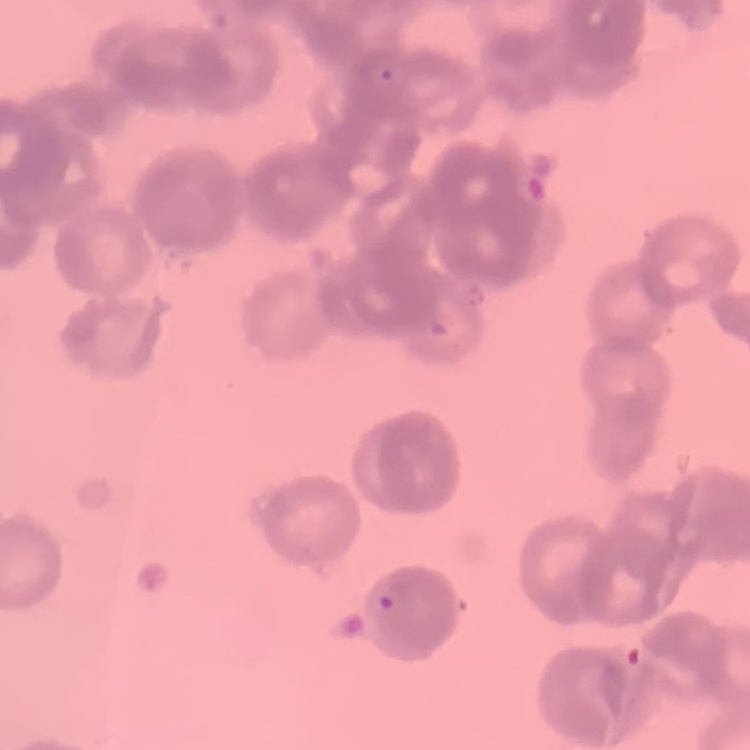
{
  "erythrocyte_morphology": "rouleaux formation",
  "stain": "Field's or Giemsa",
  "image_type": "square crop of a larger photomicrograph",
  "preparation": "thin peripheral smear"
}